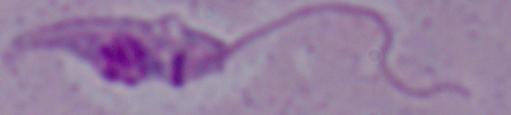

A Leishmania parasite is seen. 1000x magnification. Photomicrograph.